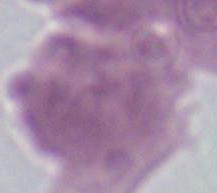

identification = red blood cell
magnification = 1000x
modality = photomicrograph